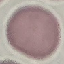
malaria_status: uninfected
stain: Giemsa
capture: smartphone through the microscope eyepiece
preparation: thin smear
image_type: cell patch, automatically extracted from a larger field of view and resized to 64 × 64 pixels